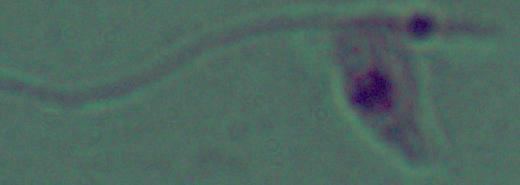 1000x magnification. Photomicrograph. A Leishmania parasite is seen.